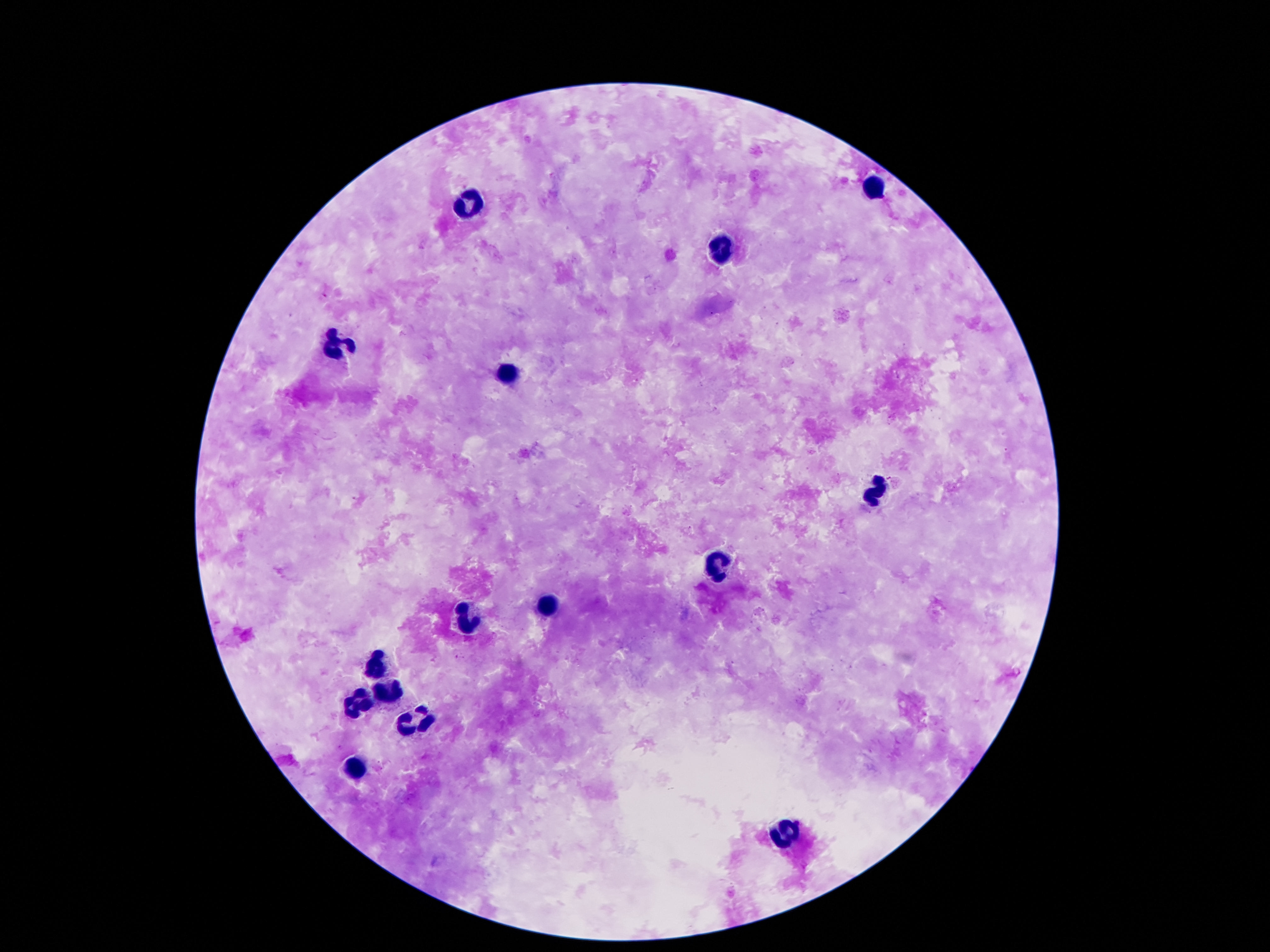

Approximate centers as (x, y) in pixels. Leukocyte locations: (873, 187), (465, 204), (719, 248), (335, 345), (503, 376), (875, 490), (719, 565), (549, 605), (466, 621), (375, 664), (384, 692), (358, 704), (413, 721), (354, 770), (783, 832). Giemsa stain. Single field of view. Image is 1270×952 pixels. Patient malaria status: uninfected. Thick peripheral-blood smear. Photographed through the microscope eyepiece with a smartphone camera. 100x magnification.